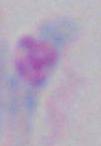
magnification = 1000x
identification = Toxoplasma gondii
modality = micrograph